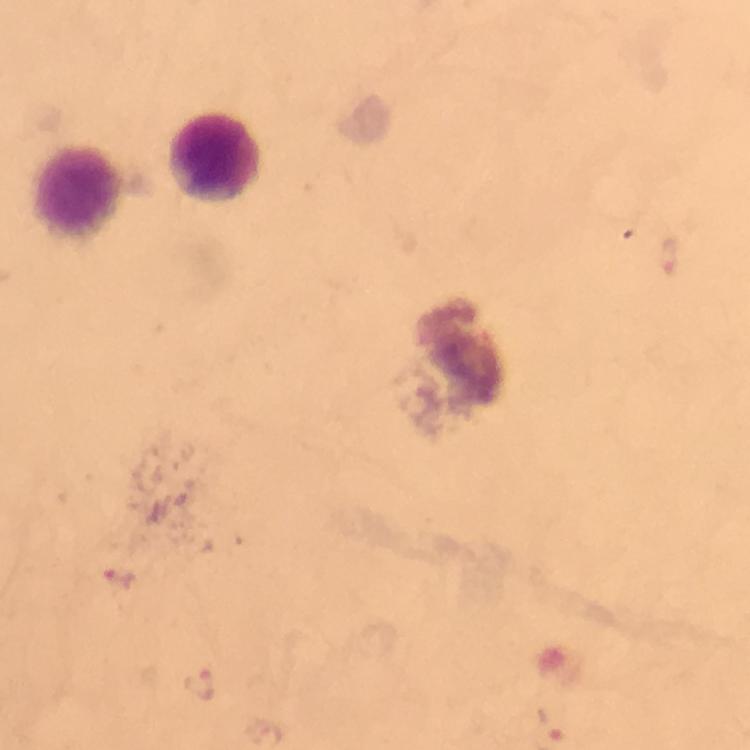
preparation = thick smear
capture = smartphone camera through the microscope
image size = 750×750 pixels
leukocyte locations = approximate centers as {x, y} in pixels: {216, 160}, {80, 194}
malaria parasite locations = approximate centers as {x, y} in pixels: {116, 579}, {198, 686}
magnification = 100x
immersion oil = applied
cropped from = a single field of view
context = from a diagnostic examination for malaria
stain = Giemsa